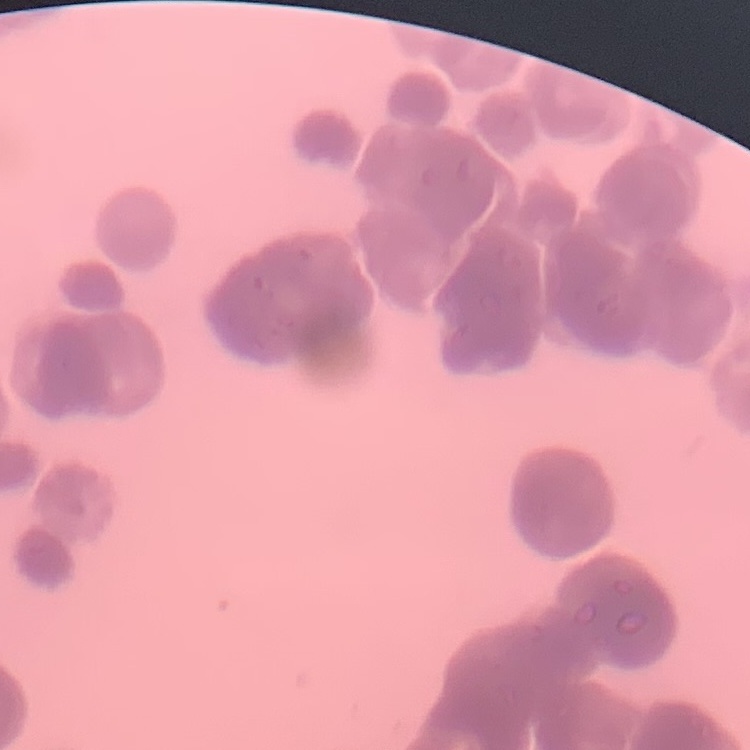

The red blood cells show rouleaux formation. One tile cut from a larger photomicrograph. Stained with either Field's or Giemsa. Thin blood smear.